State which cell type is depicted.
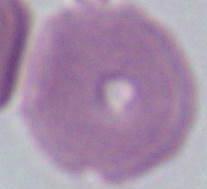
An erythrocyte.

magnification = 1000x
modality = photomicrograph